Classify this cell by malaria status.
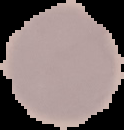
It is uninfected.

Segmented cell region on a black background. From a thin blood film. Image is 124×130 pixels.